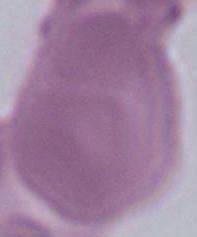
modality = photomicrograph
magnification = 1000x
identification = erythrocyte